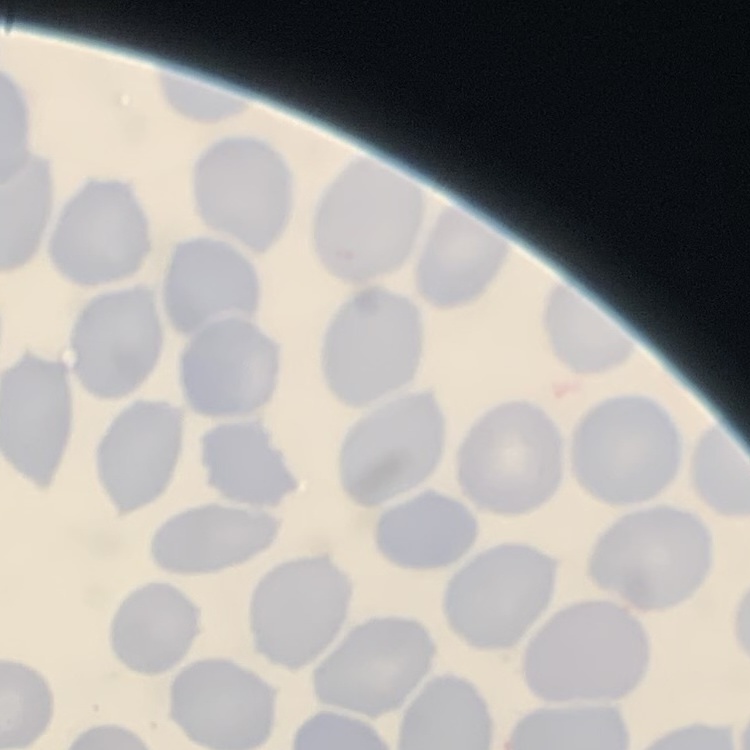

Summary:
  - Erythrocyte morphology: no rouleaux formation
  - Preparation: thin blood film
  - Image type: square crop of a larger photomicrograph
  - Stain: Field's or Giemsa